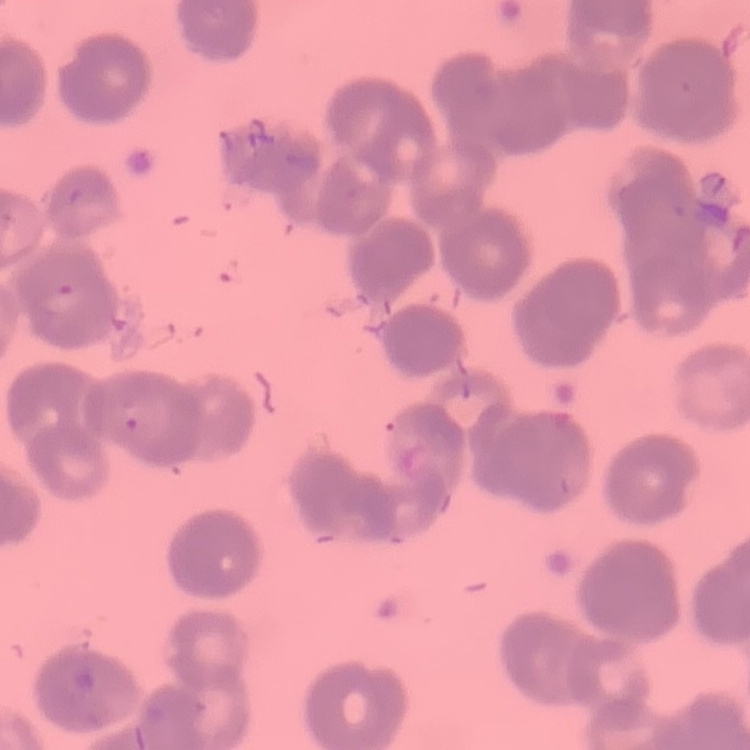

Summary:
  - Red blood cell morphology: rouleaux formation
  - Stain: Field's or Giemsa
  - Image type: square crop of a larger photomicrograph
  - Preparation: thin peripheral smear